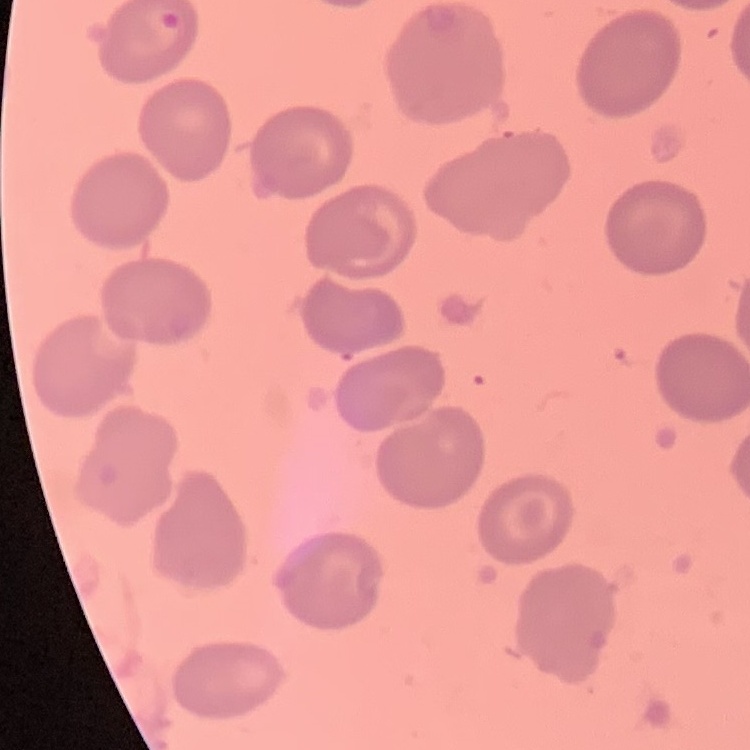
Summary:
  - Red blood cell morphology: no rouleaux formation
  - Preparation: thin blood film
  - Image type: one tile cut from a larger photomicrograph
  - Stain: Field's or Giemsa